Classify this cell by malaria status.
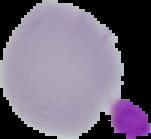

Uninfected.

Summary:
  - Image type: segmented cell region on a black background
  - Preparation: thin blood film
  - Image size: 151×139 pixels